Name the blood parasite species.
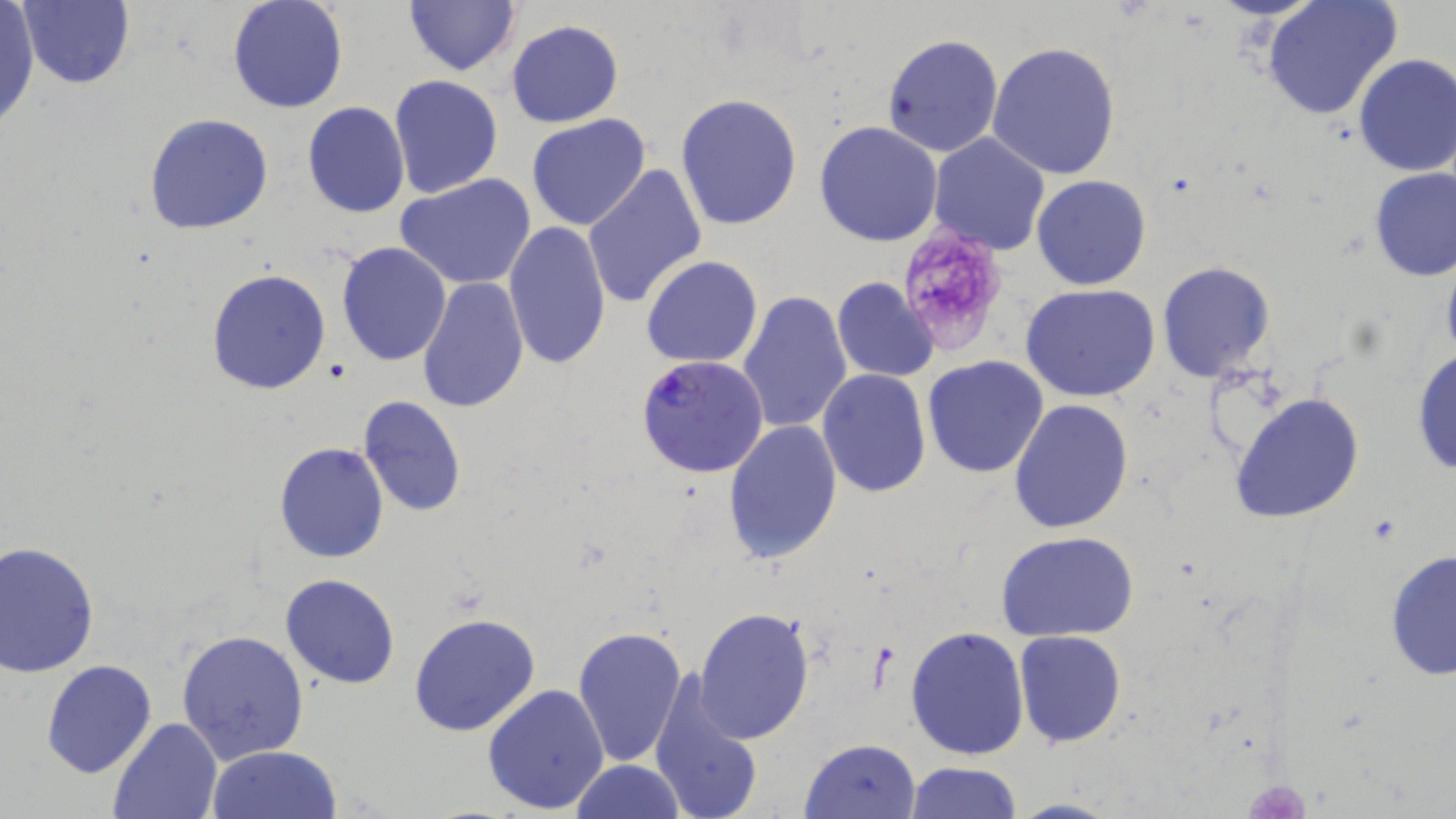

Plasmodium falciparum.

Summary:
  - Coordinate format: approximate bounding boxes as [x1, y1, x2, y2] in pixels
  - Platelet locations: [897, 224, 1014, 356], [1241, 776, 1312, 817]
  - Plasmodium falciparum-infected red blood cell locations: [637, 354, 769, 479]
  - Uninfected red blood cell locations: [20, 0, 136, 89], [402, 0, 521, 78], [1262, 0, 1403, 121], [226, 1, 349, 115], [0, 3, 39, 131], [506, 20, 625, 129], [882, 32, 1003, 158], [988, 42, 1122, 180], [1352, 54, 1456, 177], [388, 74, 504, 200], [675, 93, 803, 231], [302, 102, 410, 218], [143, 113, 274, 234], [526, 113, 652, 231], [814, 120, 944, 246], [929, 133, 1052, 257], [584, 163, 709, 309], [1369, 167, 1455, 282], [394, 174, 539, 292], [1032, 175, 1152, 291], [503, 220, 611, 371], [335, 242, 452, 367], [641, 254, 763, 368], [1157, 262, 1276, 383], [206, 269, 331, 395], [417, 275, 528, 413], [831, 277, 940, 382], [1021, 283, 1162, 402], [736, 289, 853, 435], [1411, 347, 1456, 479], [922, 356, 1050, 478], [818, 368, 931, 499], [1228, 390, 1368, 524], [358, 395, 467, 517], [1008, 400, 1134, 536], [723, 419, 844, 563], [274, 442, 388, 564], [995, 531, 1142, 641], [1, 541, 99, 677], [1384, 550, 1455, 682], [280, 573, 401, 690], [693, 607, 815, 743], [409, 611, 541, 738], [906, 624, 1032, 761], [572, 625, 687, 767], [177, 627, 309, 765], [1014, 630, 1126, 747], [42, 659, 158, 779], [649, 672, 764, 819], [481, 683, 610, 815], [107, 716, 223, 819], [800, 736, 923, 818], [208, 745, 342, 819], [570, 759, 686, 819], [902, 760, 1020, 818], [1007, 797, 1128, 819]
  - Stain: May-Grünwald-Giemsa
  - Modality: light microscopy
  - Magnification: 1000x
  - Image size: 1456×819 pixels
  - Preparation: thin blood film
  - Field of view: single